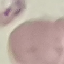
Malaria status: parasitized. Thin blood film. Giemsa stain. Photographed with a smartphone camera at the microscope eyepiece. Cell patch, automatically extracted from a larger field of view and resized to 64 × 64 pixels.